Describe the morphology of the erythrocytes.
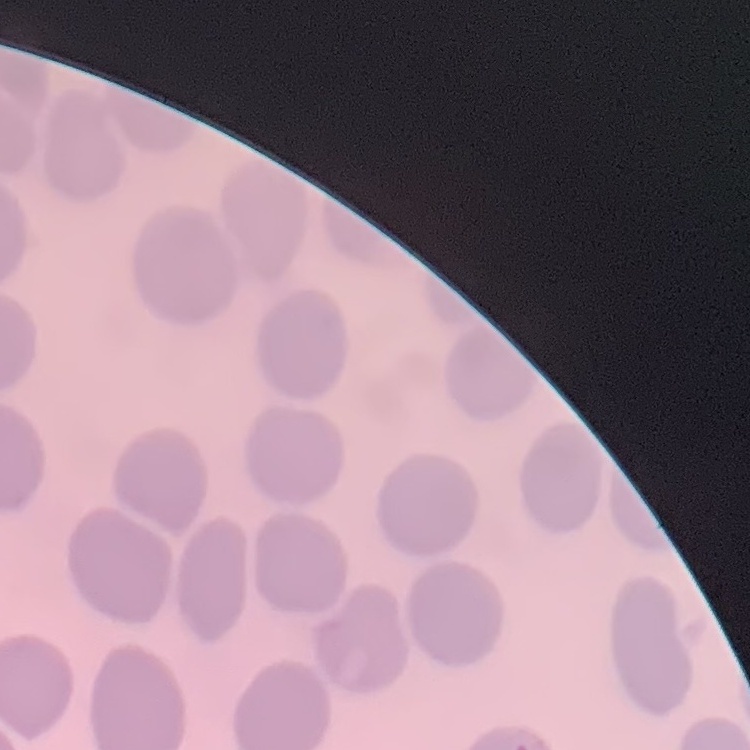
They show no rouleaux formation.

Summary:
  - Image type: one tile cut from a larger photomicrograph
  - Stain: Field's or Giemsa
  - Preparation: thin peripheral smear